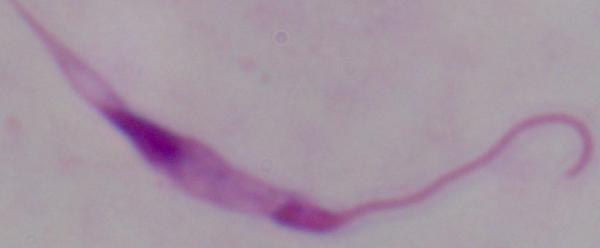

modality: photomicrograph
magnification: 1000x
identification: Leishmania